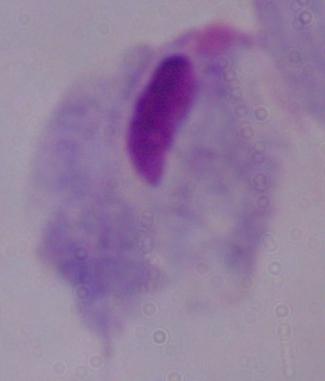

{
  "identification": "trichomonad",
  "modality": "micrograph",
  "magnification": "1000x"
}